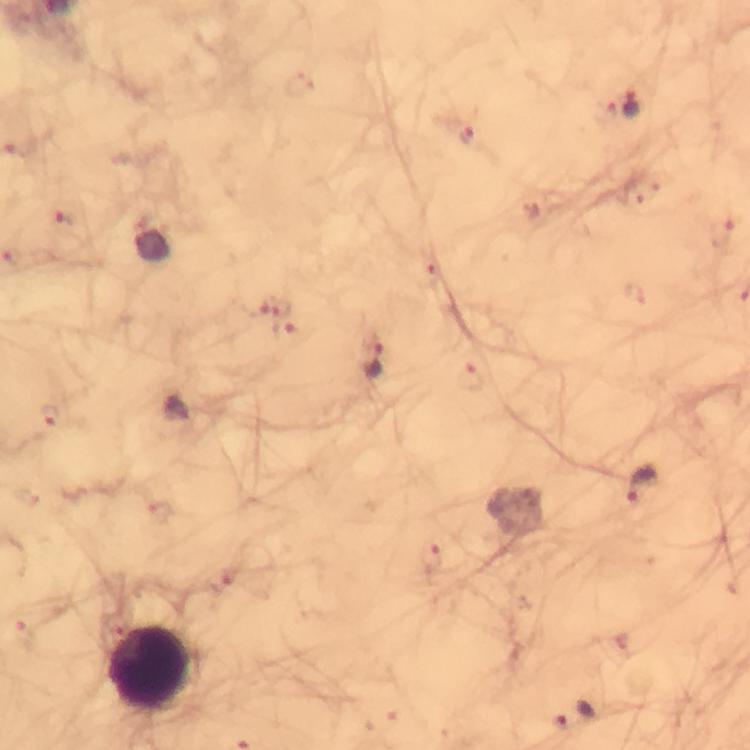
Approximate centers as {x, y} in pixels. Plasmodium parasite locations: {632, 103}, {602, 111}, {467, 135}, {69, 217}, {723, 230}, {429, 273}, {252, 303}, {282, 306}, {289, 331}, {375, 359}, {472, 379}, {48, 417}, {642, 484}, {433, 556}, {25, 632}. Leukocyte locations: {153, 670}. 100x magnification. Immersion oil applied. Photographed with a smartphone mounted on the microscope. Cropped region of a single field of view. Image is 750×750 pixels. Giemsa stain. Thick blood film. From a malaria diagnostic workup.